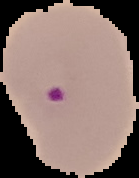

Image is 139×178 pixels. Segmented cell region on a black background. Malaria status: parasitized. From a thin blood smear.